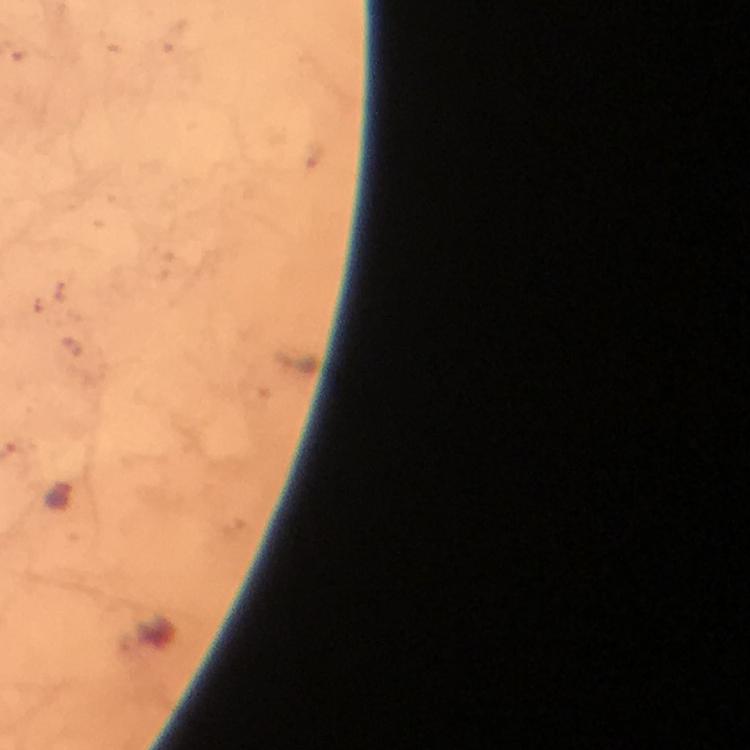
Approximate object centers, in pixels from the top-left corner.
Summary:
  - Malaria parasite locations: (x=172, y=34)
  - Image size: 750×750 pixels
  - Capture: smartphone camera through the microscope
  - Immersion oil: used
  - Preparation: thick blood film
  - Cropped from: a single field of view
  - Context: from a diagnostic examination for malaria
  - Stain: Giemsa
  - Magnification: 100x